Assess this cell for malaria.
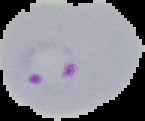
Parasitized.

From a thin blood film. Image is 145×121 pixels. Cell region segmented out of the field of view; the surrounding area is masked to black.